Point out each malaria parasite.
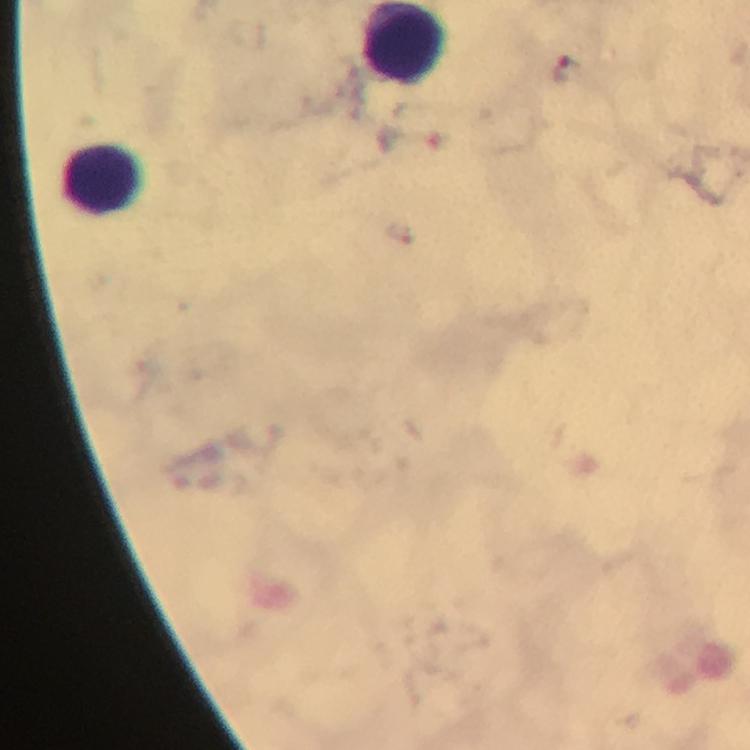

Approximate centers as (x, y) in pixels.
Malaria parasites: (562, 71), (401, 231).

Summary:
  - Leukocyte locations: (407, 42), (103, 180)
  - Immersion oil: applied
  - Cropped from: one field of view
  - Stain: Giemsa
  - Context: from a malaria diagnostic workup
  - Magnification: 100x
  - Image size: 750×750 pixels
  - Preparation: thick blood smear
  - Capture: smartphone mounted on the microscope